Name the parasite shown.
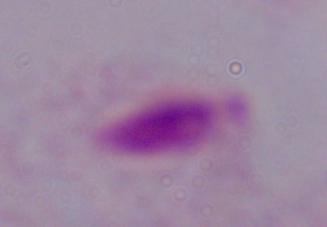

This is a trichomonad.

1000x magnification. Photomicrograph.